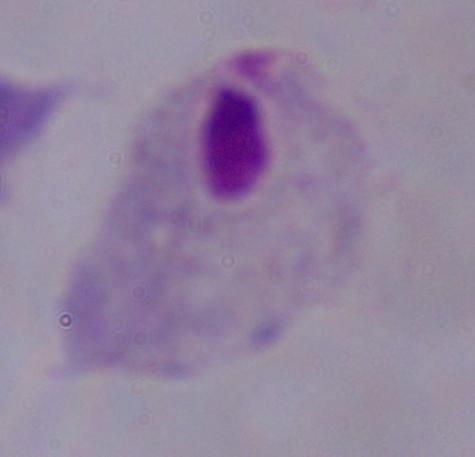

modality = photomicrograph
identification = trichomonad
magnification = 1000x